Identify the parasite.
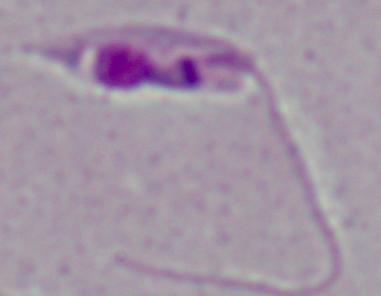

Leishmania.

Micrograph. Captured at 1000x magnification.